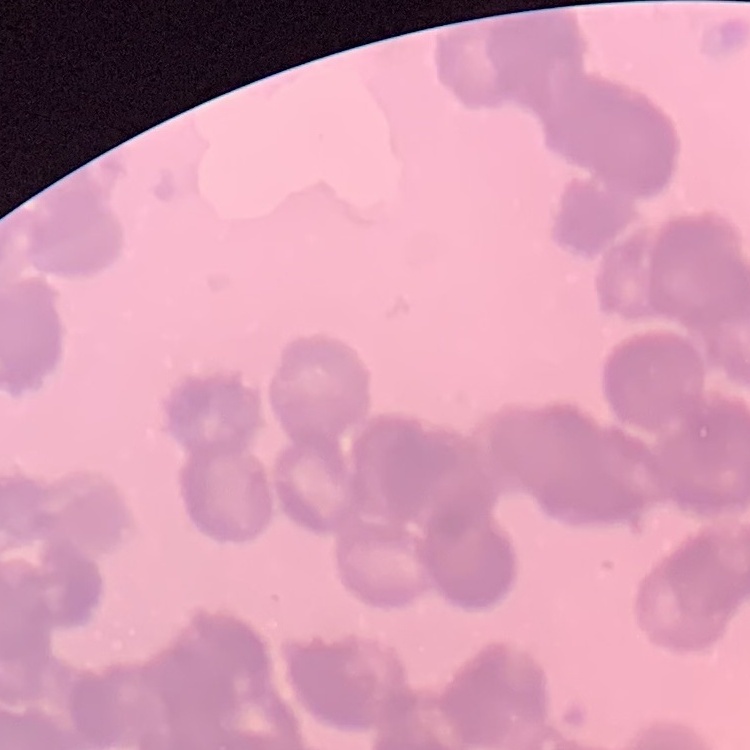

The red blood cells show rouleaux formation. Square crop of a larger photomicrograph. Thin blood smear. Stained with either Field's or Giemsa.